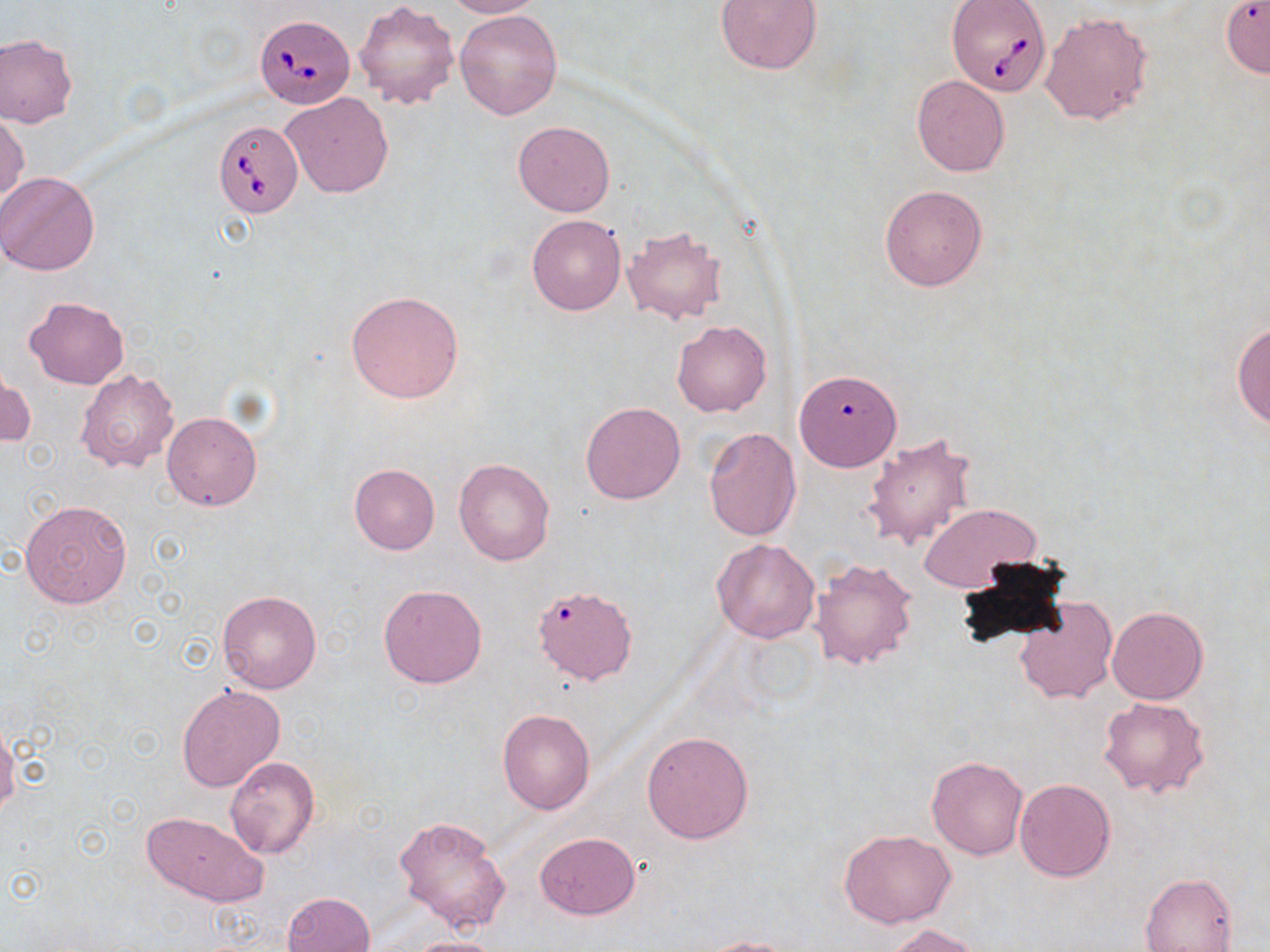
slide-level diagnosis = Babesia divergens
field of view = single
magnification = 1000x
stain = May-Grünwald-Giemsa
Babesia divergens-infected red blood cell locations = approximate bounding boxes as named x1/y1/x2/y2 corners in pixels: (x1=948, y1=0, x2=1049, y2=98), (x1=254, y1=13, x2=351, y2=108), (x1=213, y1=120, x2=302, y2=219)
uninfected red blood cell locations = approximate bounding boxes as named x1/y1/x2/y2 corners in pixels: (x1=443, y1=0, x2=542, y2=18), (x1=716, y1=0, x2=822, y2=75), (x1=354, y1=1, x2=459, y2=111), (x1=455, y1=9, x2=562, y2=120), (x1=1041, y1=12, x2=1154, y2=126), (x1=0, y1=34, x2=77, y2=129), (x1=912, y1=75, x2=1010, y2=177), (x1=280, y1=91, x2=393, y2=199), (x1=0, y1=110, x2=28, y2=207), (x1=513, y1=120, x2=615, y2=216), (x1=0, y1=171, x2=100, y2=275), (x1=879, y1=185, x2=988, y2=291), (x1=526, y1=213, x2=626, y2=315), (x1=622, y1=227, x2=727, y2=324), (x1=346, y1=291, x2=464, y2=402), (x1=25, y1=298, x2=127, y2=389), (x1=1233, y1=319, x2=1270, y2=432), (x1=672, y1=321, x2=771, y2=416), (x1=1, y1=367, x2=34, y2=450), (x1=75, y1=370, x2=180, y2=475), (x1=788, y1=375, x2=900, y2=475), (x1=580, y1=402, x2=686, y2=505), (x1=162, y1=410, x2=262, y2=511), (x1=703, y1=427, x2=801, y2=541), (x1=862, y1=431, x2=978, y2=553), (x1=454, y1=457, x2=555, y2=565), (x1=349, y1=463, x2=439, y2=554), (x1=19, y1=498, x2=131, y2=608), (x1=918, y1=503, x2=1042, y2=594), (x1=712, y1=538, x2=820, y2=644), (x1=810, y1=558, x2=919, y2=671), (x1=379, y1=584, x2=487, y2=687), (x1=217, y1=590, x2=323, y2=694), (x1=537, y1=592, x2=638, y2=691), (x1=1013, y1=597, x2=1118, y2=706), (x1=1106, y1=606, x2=1207, y2=704), (x1=177, y1=684, x2=286, y2=793), (x1=1098, y1=697, x2=1210, y2=798), (x1=497, y1=709, x2=595, y2=815), (x1=0, y1=728, x2=20, y2=813), (x1=641, y1=730, x2=755, y2=845), (x1=927, y1=755, x2=1029, y2=859), (x1=225, y1=756, x2=320, y2=859), (x1=1014, y1=777, x2=1118, y2=881), (x1=140, y1=810, x2=268, y2=905), (x1=394, y1=814, x2=511, y2=932), (x1=838, y1=829, x2=956, y2=928), (x1=534, y1=832, x2=641, y2=920), (x1=1140, y1=874, x2=1238, y2=952), (x1=282, y1=891, x2=376, y2=952), (x1=882, y1=923, x2=982, y2=952), (x1=402, y1=936, x2=507, y2=952), (x1=697, y1=937, x2=806, y2=952)
image size = 1270×952 pixels
preparation = thin blood film
modality = light microscopy